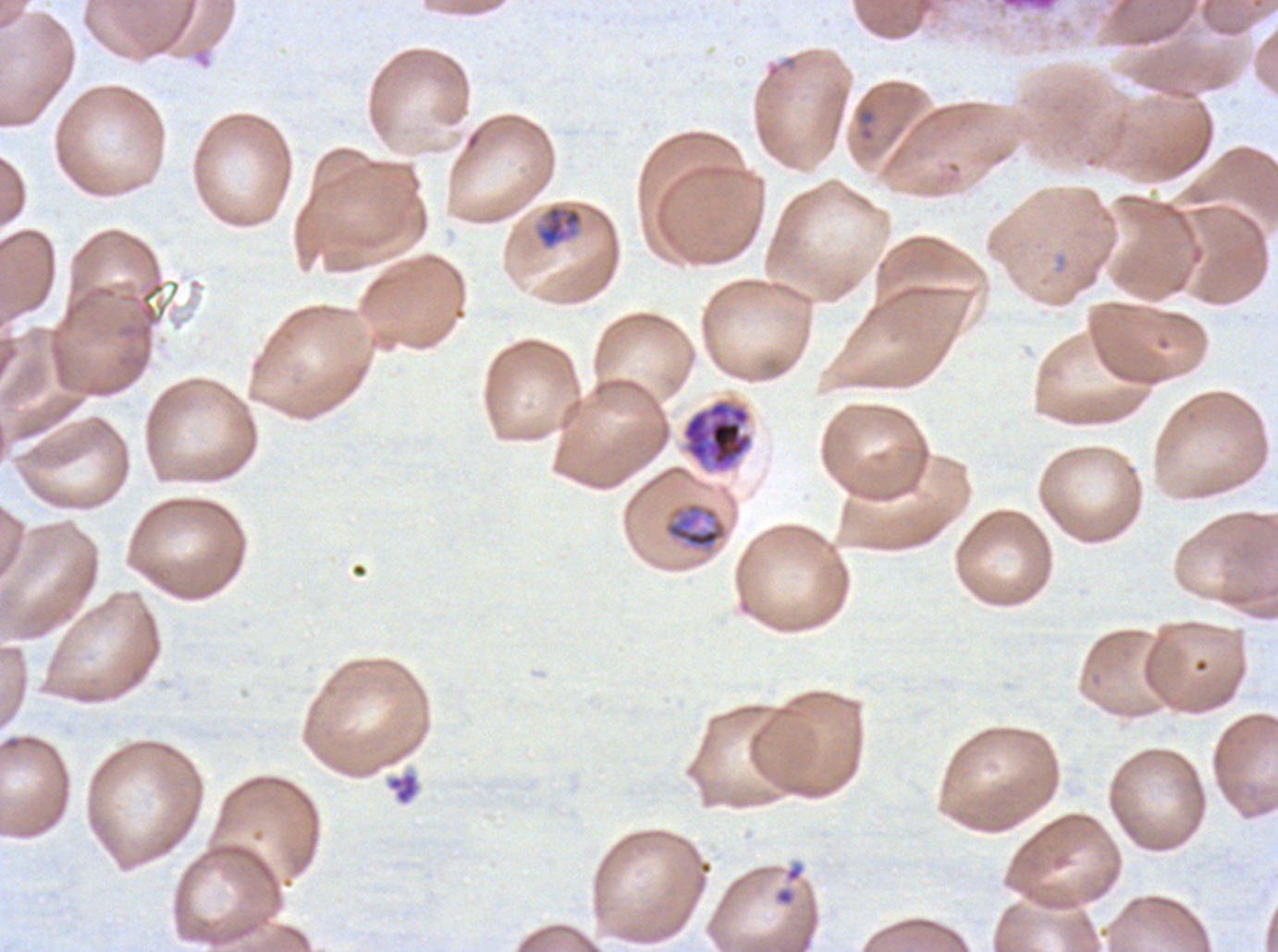
notation = approximate bounding boxes as {x1, y1, x2, y2} in pixels
ring locations = {855, 105, 877, 142}, {774, 887, 794, 906}
debris locations = {385, 770, 421, 806}
mid trophozoite locations = {663, 501, 728, 552}
late-ring/early-trophozoite locations = {535, 203, 584, 250}
late schizont locations = {682, 399, 753, 472}
life-cycle stages observed = ring, late-ring/early-trophozoite, mid trophozoite, late schizont
image size = 1278×952 pixels
field of view = sub-image separated from a larger composite
specimen = Plasmodium falciparum cultured ex vivo for 24 to 48 hours, from a patient in The Gambia
stain = Giemsa
preparation = thin blood smear